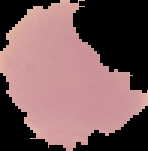

Summary:
  - Preparation: thin blood smear
  - Image type: segmented cell region with the area outside set to black
  - Malaria status: uninfected
  - Image size: 148×151 pixels